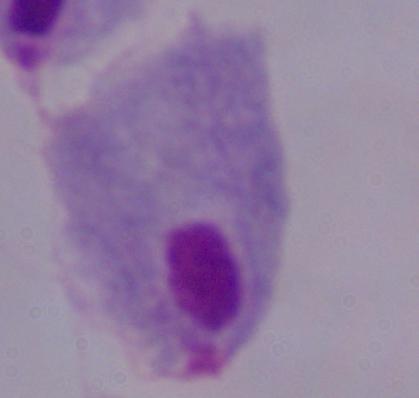
magnification = 1000x
identification = trichomonad
modality = micrograph